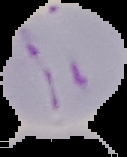 Result: malaria parasites identified. Image is 127×157 pixels. Segmented cell region on a black background. From a thin blood smear.